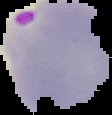

Summary:
  - Malaria status: parasitized
  - Preparation: thin blood smear
  - Image size: 112×115 pixels
  - Image type: cell region segmented out of the field of view; surrounding area masked to black